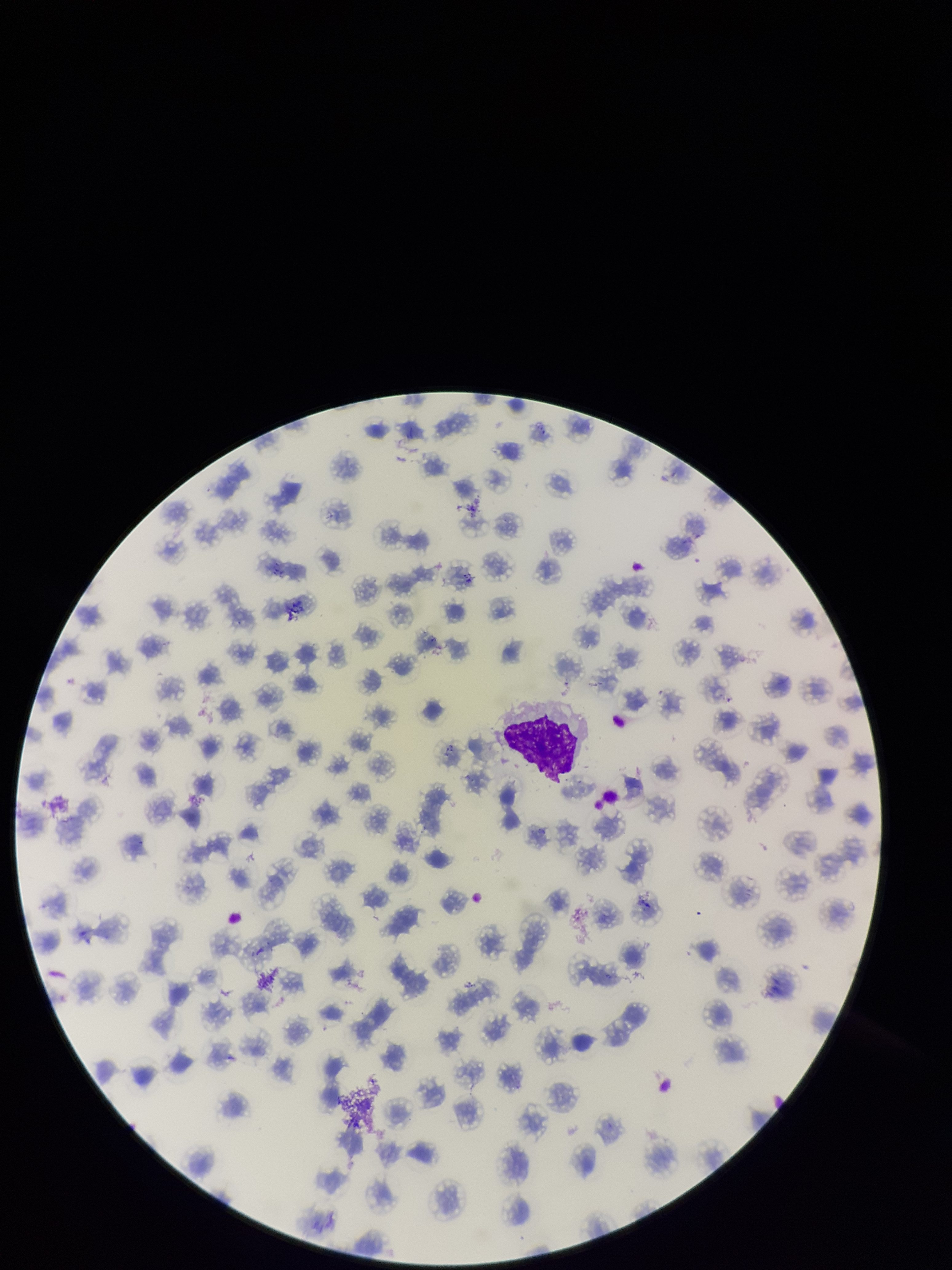
Red blood cell count: 150. Patient malaria status: positive. Parasitized red blood cells: none identified. Parasitized red blood cell count: 0. Image is 952×1270 pixels. Photographed through the microscope eyepiece with a smartphone camera. Single field of view. Preparation: thin. Stained with Giemsa. Species reported for this patient: Plasmodium falciparum.